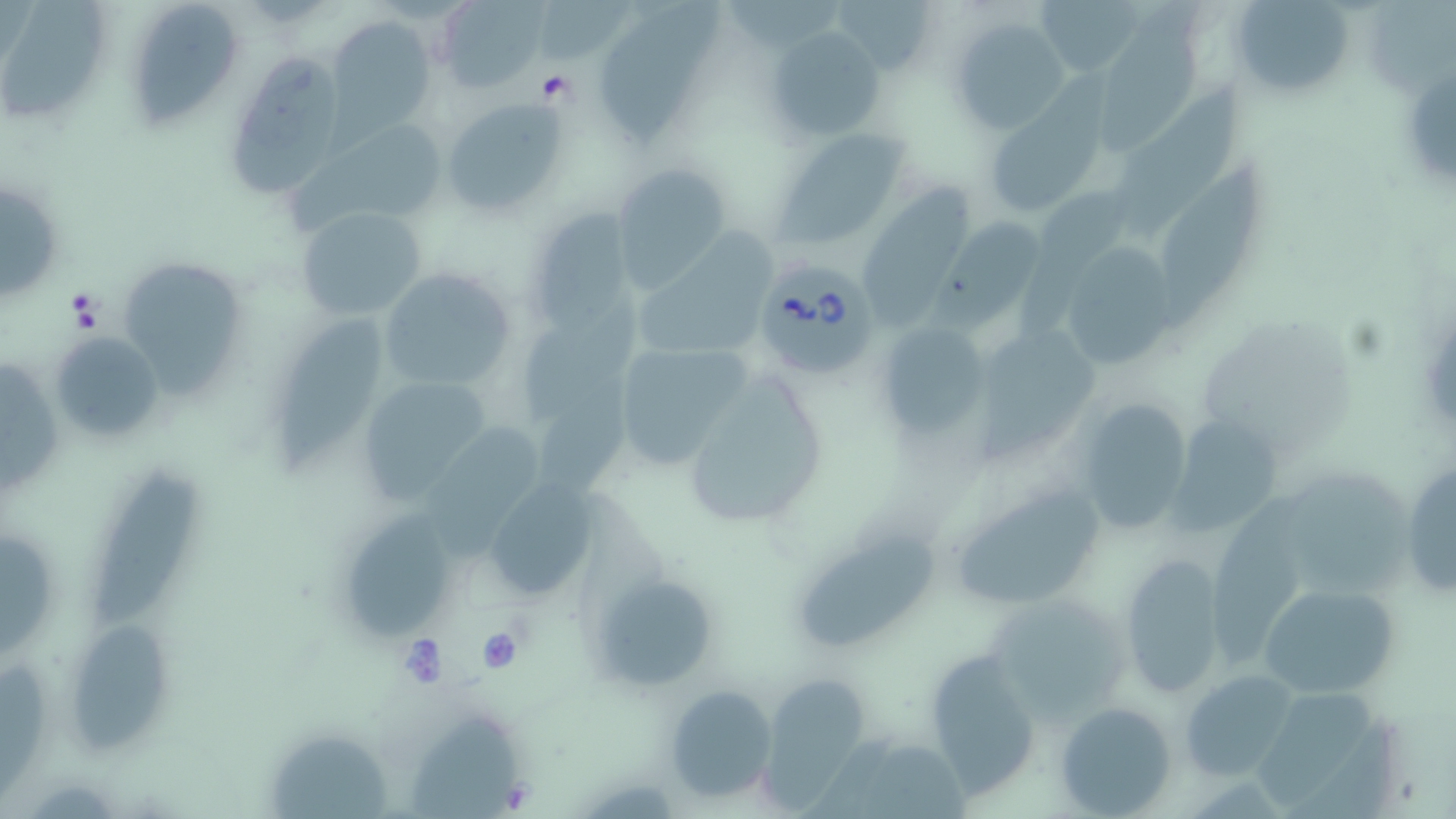

{
  "slide_level_diagnosis": "Babesia divergens",
  "modality": "optical microscopy",
  "platelet_locations": "approximate bounding boxes as (x1, y1, x2, y2) in pixels: (535, 70, 574, 104), (63, 291, 108, 334), (478, 630, 524, 672), (398, 636, 448, 685)",
  "image_size": "1456×819 pixels",
  "uninfected_red_blood_cell_locations": "approximate bounding boxes as (x1, y1, x2, y2) in pixels: (1032, 0, 1146, 80), (1105, 0, 1215, 153), (1231, 0, 1356, 100), (437, 1, 547, 91), (4, 3, 105, 118), (597, 4, 727, 143), (133, 6, 239, 122), (328, 16, 437, 136), (950, 18, 1068, 135), (768, 26, 887, 145), (223, 54, 342, 197), (1111, 88, 1252, 242), (441, 99, 567, 217), (989, 103, 1103, 219), (277, 119, 451, 231), (775, 127, 911, 244), (1161, 159, 1267, 322), (613, 164, 734, 284), (2, 182, 60, 300), (863, 183, 971, 324), (1038, 184, 1132, 274), (295, 204, 427, 323), (523, 205, 636, 334), (930, 213, 1044, 333), (643, 224, 779, 350), (1057, 240, 1183, 378), (126, 265, 243, 398), (376, 268, 520, 390), (522, 292, 642, 428), (280, 310, 385, 485), (876, 321, 990, 442), (977, 321, 1108, 461), (46, 329, 162, 445), (609, 339, 754, 468), (0, 352, 61, 492), (355, 373, 497, 501), (688, 377, 821, 521), (536, 381, 637, 499), (1072, 398, 1197, 533), (1170, 413, 1282, 533), (424, 426, 542, 558), (1399, 459, 1455, 600), (95, 468, 202, 630), (490, 481, 594, 590), (948, 483, 1110, 611), (1208, 485, 1311, 663), (351, 508, 449, 643), (0, 529, 54, 653), (797, 530, 935, 646), (1117, 555, 1229, 697), (592, 574, 719, 692), (1259, 582, 1400, 700), (77, 620, 170, 753), (922, 646, 1046, 799), (1183, 669, 1297, 781), (761, 674, 867, 803), (1257, 675, 1374, 806), (666, 685, 777, 803), (1057, 701, 1177, 817), (406, 714, 525, 819), (272, 735, 396, 819)",
  "babesia_divergens_infected_red_blood_cell_locations": "approximate bounding boxes as (x1, y1, x2, y2) in pixels: (758, 256, 884, 380)",
  "preparation": "thin blood smear",
  "stain": "May-Grünwald-Giemsa",
  "field_of_view": "one of a larger specimen",
  "magnification": "1000x"
}